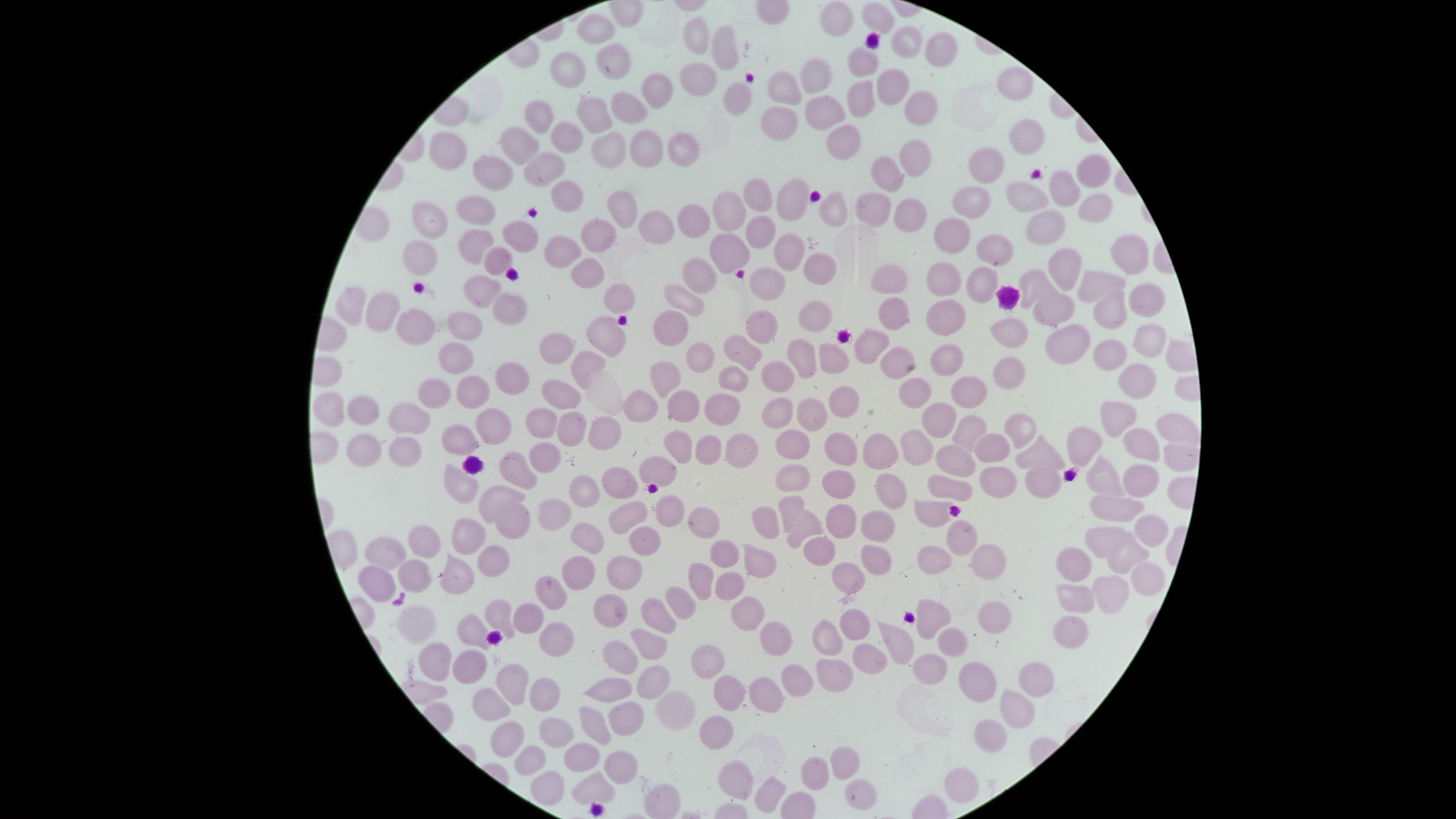 Approximate marker points as (x, y) in pixels. Uninfected red blood cells: (875, 18), (834, 20), (600, 27), (698, 35), (908, 44), (727, 47), (942, 54), (611, 59), (860, 60), (569, 70), (812, 74), (695, 77), (890, 80), (1019, 80), (780, 85), (652, 91), (731, 96), (856, 101), (926, 102), (628, 109), (594, 111), (823, 114), (543, 116), (777, 126), (566, 136), (1024, 137), (843, 141), (523, 143), (608, 144), (688, 144), (642, 148), (451, 151), (916, 154), (985, 167), (547, 169), (1092, 170), (891, 176), (496, 180), (1063, 187), (760, 195), (1021, 195), (570, 198), (792, 198), (971, 201), (731, 205), (1091, 206), (619, 209), (873, 209), (476, 211), (912, 211), (832, 214), (693, 215), (430, 217), (647, 228), (1048, 228), (758, 229), (953, 230), (517, 234), (597, 243), (472, 244), (993, 246), (788, 250), (567, 251), (727, 253), (1122, 260), (493, 261), (419, 262), (1061, 265), (818, 267), (939, 271), (699, 273), (593, 274), (891, 275), (984, 280), (772, 281), (1038, 281), (1098, 282), (481, 284), (1145, 296), (685, 299), (351, 301), (511, 303), (618, 304), (382, 305), (1057, 307), (1112, 312), (900, 314), (943, 315), (815, 316), (469, 323), (421, 326), (1016, 326), (671, 328), (607, 329), (761, 330), (1149, 339), (1064, 341), (870, 342), (743, 350), (801, 352), (950, 353), (1110, 353), (558, 354), (451, 357), (832, 357), (697, 359), (889, 363), (588, 365), (1011, 365), (732, 376), (779, 376), (508, 377), (667, 382), (1141, 382), (473, 386), (431, 387), (916, 389), (969, 392), (559, 396), (842, 396), (326, 404), (777, 404), (814, 405), (645, 406), (683, 406), (724, 406), (360, 409), (414, 413), (939, 417), (1111, 417), (491, 421), (544, 421), (1171, 425), (575, 427), (1021, 427), (969, 431), (600, 433), (463, 437), (790, 443), (996, 443), (1078, 444), (919, 445), (1143, 445), (367, 446), (411, 446), (680, 446), (704, 449), (843, 450), (882, 452), (737, 453), (1037, 454), (544, 455), (516, 464), (957, 464), (658, 465), (787, 472), (1038, 475), (617, 477), (1099, 477), (450, 482), (838, 482), (1136, 482), (954, 487), (995, 487), (585, 488), (890, 490), (497, 492), (789, 503), (664, 506), (556, 510), (1111, 510), (626, 511), (932, 512), (508, 519), (761, 520), (703, 521), (840, 524), (873, 527), (799, 531), (962, 533), (1097, 535), (1147, 535), (464, 536), (428, 538), (590, 539), (644, 543), (818, 550), (391, 551), (724, 552), (935, 552), (1125, 553), (981, 554), (763, 557), (487, 560), (874, 561), (1068, 564), (622, 566), (410, 572), (578, 573), (1142, 576), (846, 577), (456, 579), (732, 579), (375, 581), (699, 583), (551, 586), (1101, 590), (684, 599), (1069, 601), (614, 608), (742, 608), (531, 612), (501, 616), (408, 617), (987, 617), (933, 618), (655, 622), (853, 626), (465, 633), (1075, 634), (778, 636), (557, 640), (644, 642), (948, 643), (823, 646), (890, 646), (627, 657), (709, 660), (435, 661), (861, 662), (465, 664), (928, 667), (1036, 670), (790, 671), (832, 674), (512, 679), (653, 680), (981, 685), (609, 686), (540, 692), (728, 693), (764, 693), (491, 696), (1017, 704), (627, 715), (684, 715), (716, 726), (595, 729), (989, 732), (553, 733), (513, 739), (584, 758), (527, 760), (846, 761), (625, 767), (820, 768), (738, 780), (962, 782), (590, 788), (546, 792), (766, 794), (856, 794). Photographed with a smartphone camera through the microscope eyepiece. Thin blood smear. Image is 1456×819 pixels. Single field of view. Circular visible region. Giemsa-stained preparation. Presence: no malaria parasites detected.